Report the malaria status of this cell.
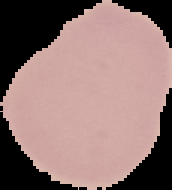
Uninfected.

Cell region segmented out of the field of view; the surrounding area is masked to black. Image is 172×190 pixels. From a thin blood film.